State which parasite is depicted.
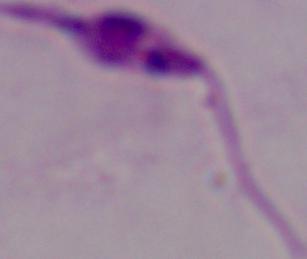
This is Leishmania.

modality: micrograph
magnification: 1000x